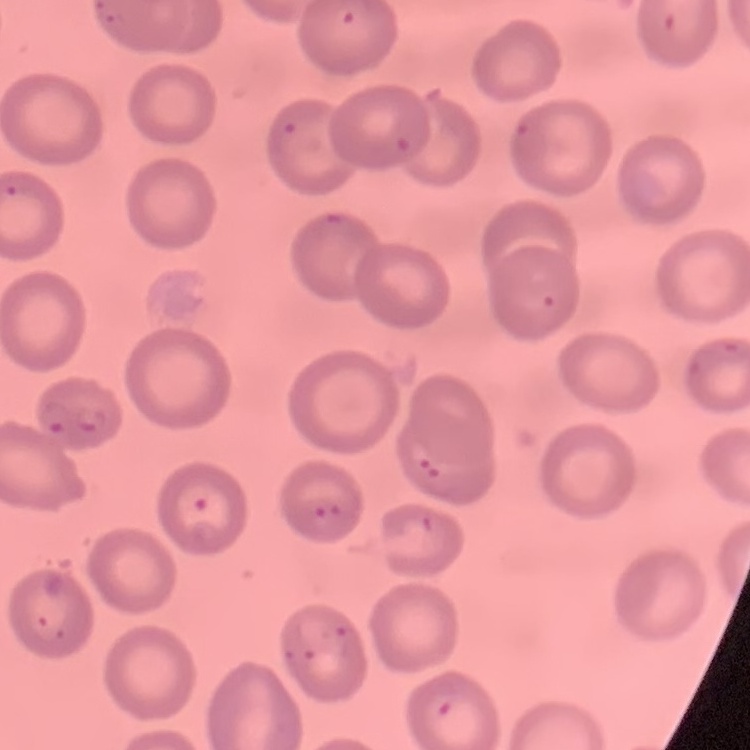

red_blood_cell_morphology: no rouleaux formation
preparation: thin peripheral smear
stain: Field's or Giemsa
image_type: one tile cut from a larger photomicrograph